Describe the morphology of the erythrocytes.
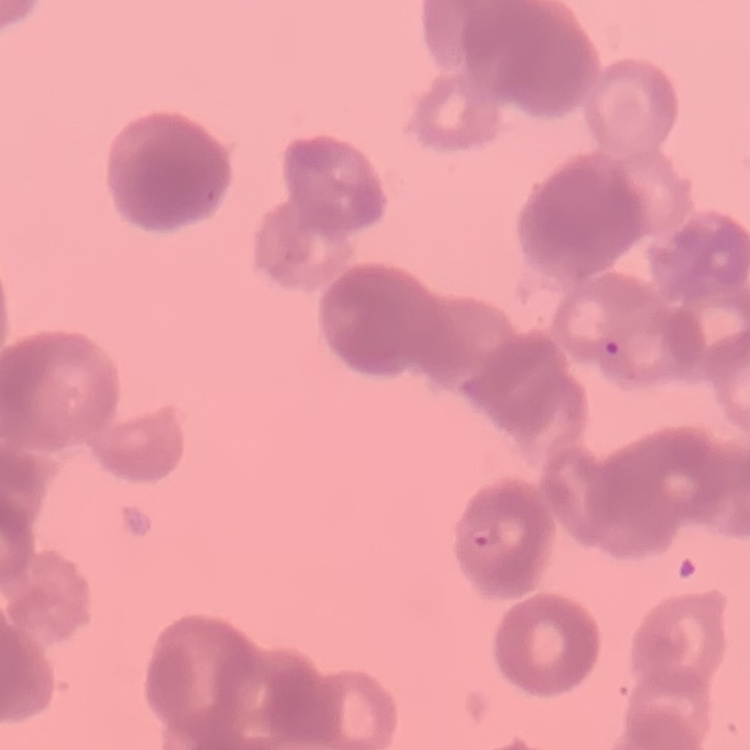
Rouleaux formation.

preparation = thin peripheral smear
stain = Field's or Giemsa
image type = square crop of a larger photomicrograph